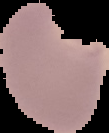

Summary:
  - Preparation: thin blood smear
  - Image type: segmented cell region with the area outside set to black
  - Result: Plasmodium parasites detected
  - Image size: 109×133 pixels